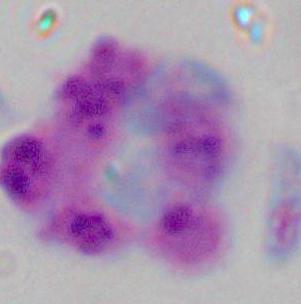

Summary:
  - Modality: photomicrograph
  - Identification: white blood cell
  - Magnification: 1000x